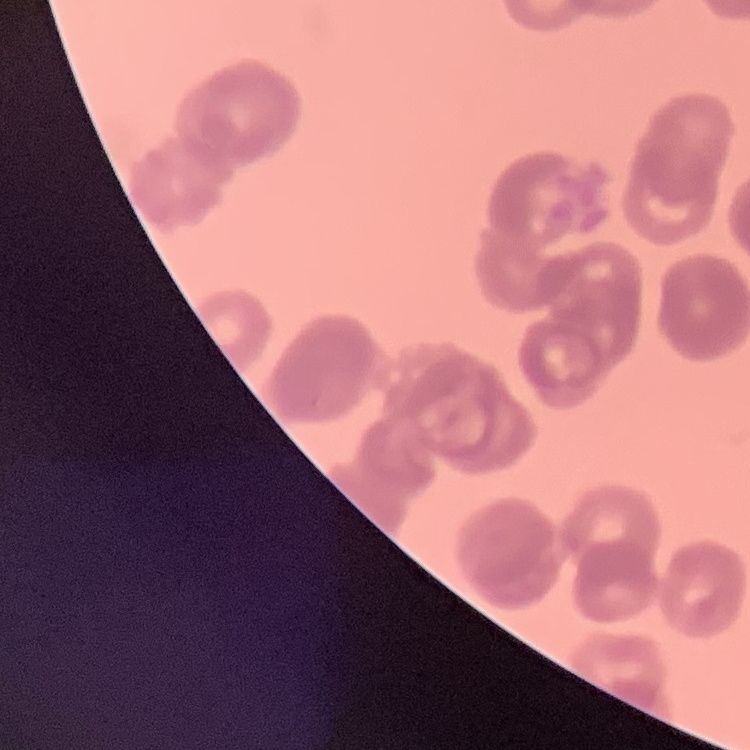

{
  "red_blood_cell_morphology": "rouleaux formation",
  "stain": "Field's or Giemsa",
  "image_type": "one tile cut from a larger photomicrograph",
  "preparation": "thin blood smear"
}